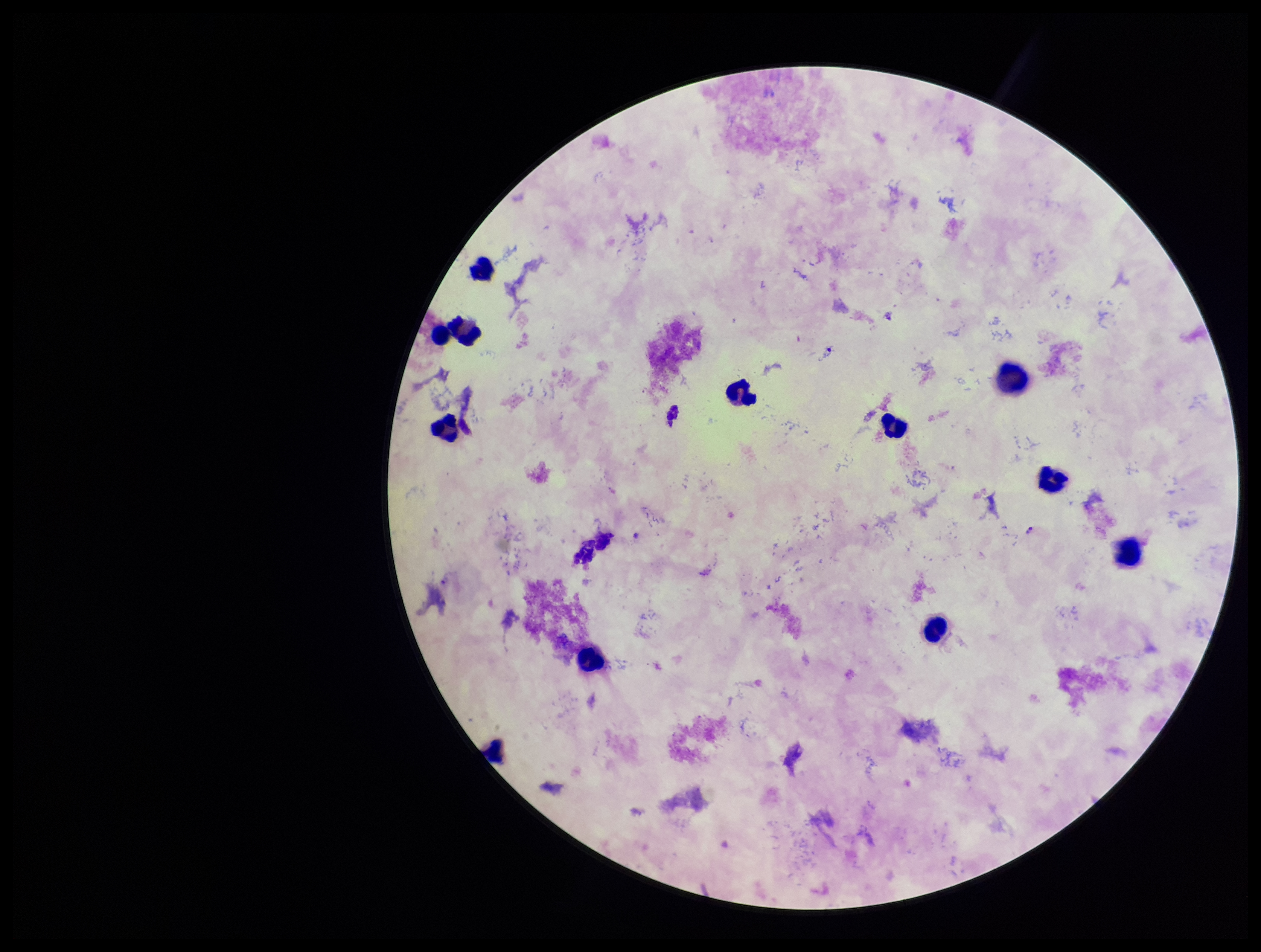

Summary:
  - Patient malaria status: infected
  - Preparation: thick smear
  - Species reported for this patient: Plasmodium falciparum
  - Stain: Giemsa
  - Leukocyte count: 12
  - Capture: smartphone photograph through the microscope eyepiece
  - Field of view: single
  - Parasite count: 1
  - Plasmodium parasites: seen
  - Image size: 1261×952 pixels